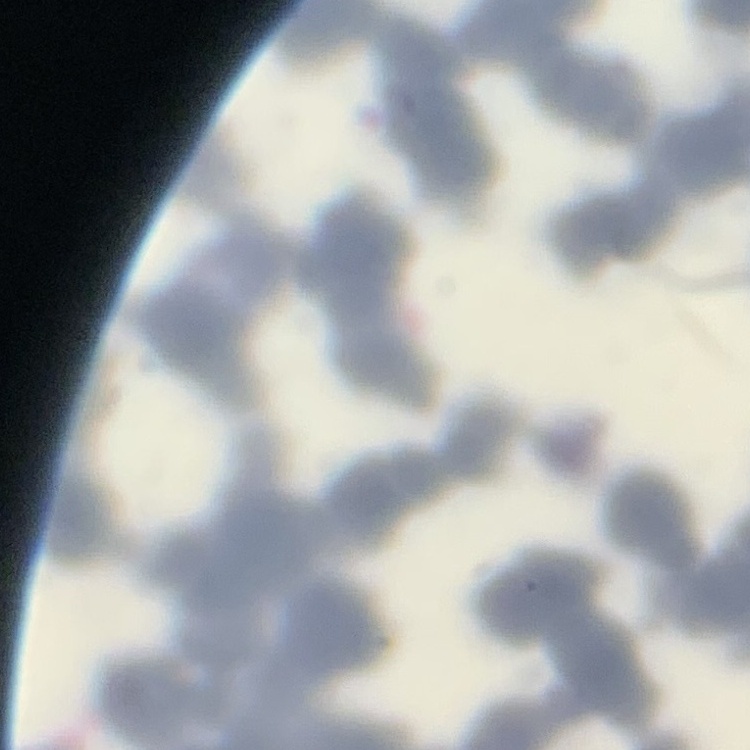
The erythrocytes exhibit rouleaux formation. Stained with either Field's or Giemsa. Thin blood smear. One tile cut from a larger photomicrograph.